Report the malaria status of this cell.
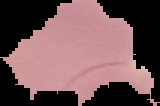

It is uninfected.

image size = 160×106 pixels
preparation = thin blood smear
image type = segmented cell region on a black background